Classify this cell by malaria status.
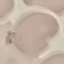
It is uninfected.

{
  "preparation": "thin blood smear",
  "stain": "Giemsa",
  "capture": "smartphone through the microscope eyepiece",
  "image_type": "automatically extracted cell patch, resized to 64 × 64 pixels"
}